Name the blood parasite species.
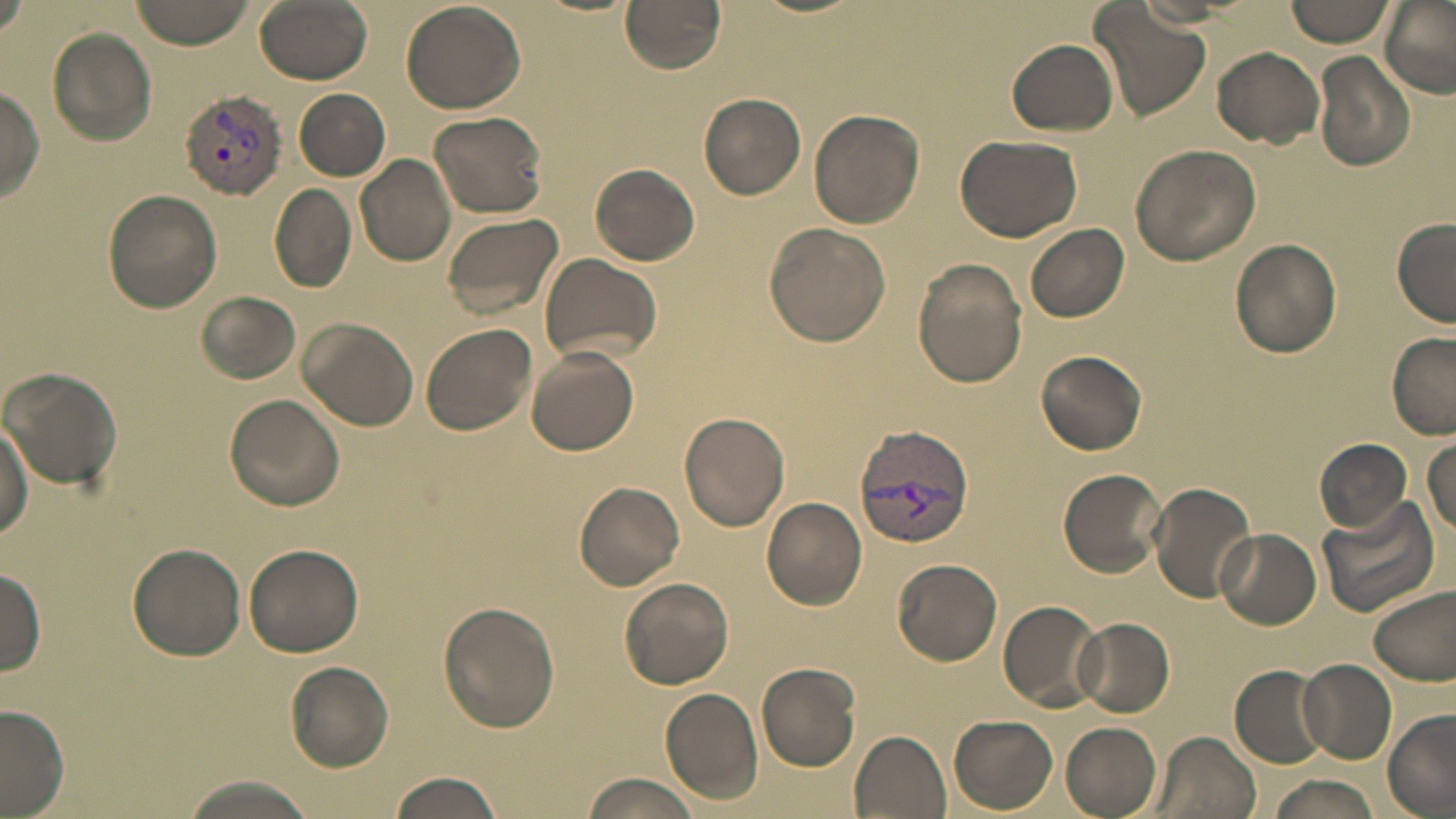

Plasmodium vivax.

{
  "field_of_view": "single",
  "image_size": "1456×819 pixels",
  "preparation": "thin blood film",
  "modality": "optical microscopy",
  "uninfected_red_blood_cell_locations": "approximate bounding boxes as [x1, y1, x2, y2] in pixels: [0, 0, 33, 39], [130, 0, 258, 50], [252, 0, 373, 83], [620, 0, 727, 73], [1087, 0, 1209, 120], [1284, 0, 1394, 46], [1377, 1, 1456, 100], [401, 2, 525, 114], [47, 27, 157, 147], [1006, 38, 1118, 137], [1212, 46, 1325, 146], [1314, 51, 1417, 170], [0, 83, 45, 202], [295, 88, 389, 179], [698, 93, 807, 198], [809, 108, 924, 227], [429, 109, 547, 217], [954, 134, 1082, 241], [1129, 143, 1260, 265], [354, 154, 457, 266], [590, 164, 699, 266], [271, 184, 356, 293], [103, 189, 221, 313], [440, 210, 565, 322], [1392, 219, 1455, 327], [764, 222, 892, 349], [1027, 223, 1129, 323], [1230, 237, 1343, 358], [537, 252, 662, 364], [912, 260, 1025, 389], [196, 290, 300, 384], [297, 316, 420, 432], [419, 322, 538, 435], [1386, 332, 1456, 438], [526, 346, 639, 455], [1036, 349, 1146, 456], [1, 366, 122, 492], [225, 394, 345, 510], [679, 411, 790, 530], [0, 420, 32, 540], [1314, 438, 1411, 533], [1426, 439, 1456, 538], [1057, 467, 1169, 577], [574, 481, 685, 589], [1147, 481, 1256, 604], [761, 497, 867, 609], [1315, 498, 1440, 617], [1215, 528, 1322, 629], [127, 543, 246, 659], [243, 544, 363, 657], [892, 558, 1003, 666], [0, 564, 46, 676], [620, 577, 734, 689], [1370, 583, 1456, 686], [999, 600, 1101, 711], [439, 601, 560, 732], [1074, 616, 1175, 717], [1296, 658, 1397, 764], [285, 661, 395, 771], [755, 661, 862, 771], [1230, 664, 1332, 768], [661, 689, 763, 804], [0, 705, 71, 817], [1384, 711, 1456, 818], [949, 715, 1058, 812], [1060, 723, 1162, 817], [849, 730, 952, 818], [1148, 730, 1258, 819], [385, 772, 507, 819], [577, 772, 704, 819], [177, 776, 316, 819], [1267, 776, 1385, 819]",
  "stain": "May-Grünwald-Giemsa",
  "plasmodium_vivax_infected_red_blood_cell_locations": "approximate bounding boxes as [x1, y1, x2, y2] in pixels: [179, 89, 286, 197], [852, 426, 974, 550]",
  "magnification": "1000x"
}